Outline each blood parasite and name the species.
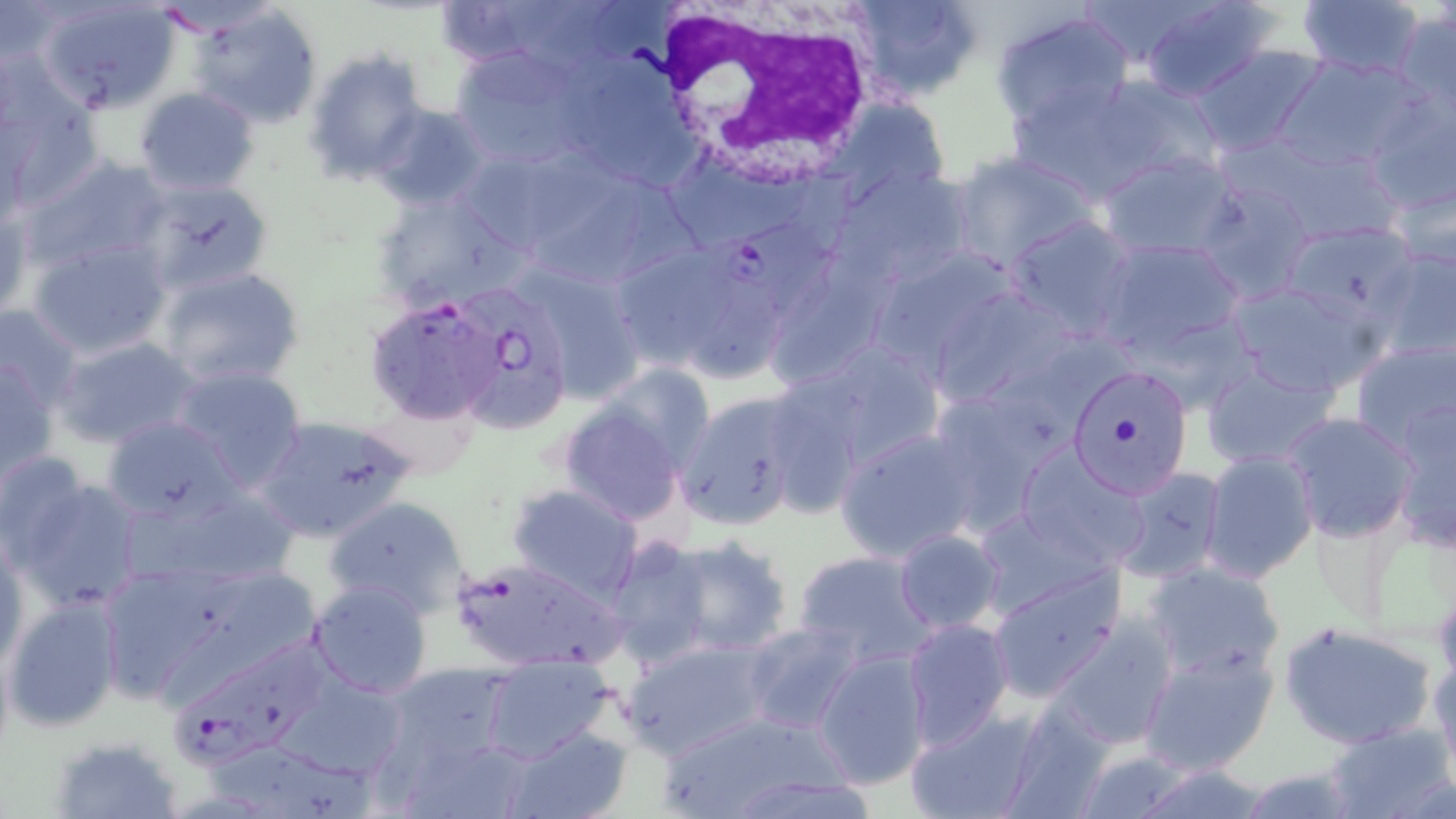

Approximate bounding boxes as named x1/y1/x2/y2 corners in pixels.
Plasmodium falciparum-infected red blood cells: (x1=711, y1=218, x2=841, y2=315), (x1=454, y1=290, x2=577, y2=433), (x1=364, y1=296, x2=502, y2=425), (x1=449, y1=558, x2=625, y2=673), (x1=181, y1=631, x2=345, y2=771).
No Plasmodium ovale, Plasmodium malariae, Plasmodium vivax, Babesia divergens, or Trypanosoma brucei observed.

Uninfected red blood cell locations: (x1=36, y1=0, x2=183, y2=114), (x1=848, y1=0, x2=986, y2=104), (x1=1079, y1=0, x2=1211, y2=70), (x1=1135, y1=0, x2=1283, y2=103), (x1=434, y1=1, x2=575, y2=69), (x1=1295, y1=1, x2=1427, y2=81), (x1=186, y1=3, x2=324, y2=130), (x1=990, y1=9, x2=1133, y2=131), (x1=1390, y1=11, x2=1456, y2=123), (x1=1192, y1=44, x2=1327, y2=159), (x1=450, y1=46, x2=592, y2=169), (x1=303, y1=49, x2=430, y2=184), (x1=554, y1=54, x2=696, y2=185), (x1=1273, y1=54, x2=1427, y2=176), (x1=1, y1=70, x2=101, y2=209), (x1=1087, y1=73, x2=1223, y2=185), (x1=1005, y1=79, x2=1156, y2=202), (x1=135, y1=87, x2=260, y2=196), (x1=1363, y1=90, x2=1456, y2=217), (x1=822, y1=95, x2=955, y2=197), (x1=372, y1=104, x2=495, y2=211), (x1=1247, y1=135, x2=1412, y2=249), (x1=947, y1=149, x2=1100, y2=272), (x1=512, y1=150, x2=687, y2=287), (x1=1097, y1=151, x2=1242, y2=262), (x1=24, y1=155, x2=171, y2=272), (x1=833, y1=168, x2=975, y2=287), (x1=1383, y1=168, x2=1456, y2=273), (x1=136, y1=177, x2=274, y2=293), (x1=1193, y1=179, x2=1317, y2=306), (x1=370, y1=190, x2=520, y2=310), (x1=0, y1=196, x2=32, y2=318), (x1=1004, y1=216, x2=1139, y2=342), (x1=1277, y1=221, x2=1425, y2=330), (x1=26, y1=235, x2=173, y2=357), (x1=1095, y1=236, x2=1248, y2=359), (x1=865, y1=241, x2=1032, y2=381), (x1=611, y1=244, x2=727, y2=370), (x1=1372, y1=244, x2=1456, y2=367), (x1=763, y1=257, x2=891, y2=392), (x1=522, y1=265, x2=647, y2=404), (x1=158, y1=266, x2=305, y2=390), (x1=1223, y1=279, x2=1387, y2=400), (x1=674, y1=281, x2=788, y2=391), (x1=926, y1=284, x2=1085, y2=418), (x1=0, y1=303, x2=85, y2=412), (x1=55, y1=336, x2=201, y2=450), (x1=1349, y1=337, x2=1455, y2=453), (x1=790, y1=338, x2=947, y2=474), (x1=1199, y1=354, x2=1342, y2=471), (x1=1, y1=356, x2=58, y2=481), (x1=170, y1=365, x2=308, y2=494), (x1=1066, y1=365, x2=1193, y2=498), (x1=923, y1=387, x2=1065, y2=535), (x1=674, y1=391, x2=811, y2=532), (x1=360, y1=394, x2=474, y2=482), (x1=1388, y1=397, x2=1455, y2=551), (x1=558, y1=400, x2=690, y2=526), (x1=1282, y1=412, x2=1418, y2=542), (x1=101, y1=414, x2=243, y2=523), (x1=254, y1=414, x2=416, y2=542), (x1=834, y1=426, x2=984, y2=563), (x1=1014, y1=442, x2=1153, y2=570), (x1=1200, y1=450, x2=1318, y2=583), (x1=0, y1=451, x2=92, y2=563), (x1=1111, y1=465, x2=1228, y2=582), (x1=12, y1=475, x2=148, y2=611), (x1=508, y1=482, x2=642, y2=602), (x1=120, y1=484, x2=300, y2=591), (x1=322, y1=496, x2=471, y2=621), (x1=894, y1=528, x2=1005, y2=635), (x1=1, y1=532, x2=27, y2=668), (x1=654, y1=534, x2=797, y2=658), (x1=604, y1=537, x2=718, y2=666), (x1=794, y1=549, x2=938, y2=669), (x1=92, y1=560, x2=281, y2=708), (x1=1143, y1=562, x2=1287, y2=683), (x1=987, y1=567, x2=1125, y2=702), (x1=308, y1=579, x2=434, y2=700), (x1=5, y1=593, x2=124, y2=731), (x1=1049, y1=615, x2=1178, y2=749), (x1=903, y1=617, x2=1014, y2=748), (x1=739, y1=621, x2=864, y2=734), (x1=1278, y1=621, x2=1438, y2=749), (x1=620, y1=636, x2=776, y2=757), (x1=1137, y1=641, x2=1281, y2=775), (x1=810, y1=647, x2=933, y2=790), (x1=1430, y1=647, x2=1456, y2=788), (x1=479, y1=656, x2=619, y2=766), (x1=382, y1=663, x2=517, y2=773), (x1=273, y1=668, x2=420, y2=775), (x1=992, y1=697, x2=1121, y2=819), (x1=902, y1=705, x2=1044, y2=819), (x1=655, y1=709, x2=851, y2=819), (x1=1321, y1=719, x2=1456, y2=819), (x1=501, y1=724, x2=633, y2=819), (x1=51, y1=735, x2=186, y2=818), (x1=212, y1=740, x2=374, y2=818). White blood cell locations: (x1=644, y1=2, x2=882, y2=184). Slide-level diagnosis: Plasmodium falciparum. May-Grünwald-Giemsa-stained preparation. 1000x magnification. Image is 1456×819 pixels. Thin blood film. Optical microscopy. One field of a larger specimen.